Report the malaria status of this cell.
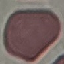

Uninfected.

Summary:
  - Image type: cell patch, automatically extracted from a larger field of view and resized to 64 × 64 pixels
  - Capture: smartphone camera at the microscope eyepiece
  - Stain: Giemsa
  - Preparation: thin blood film